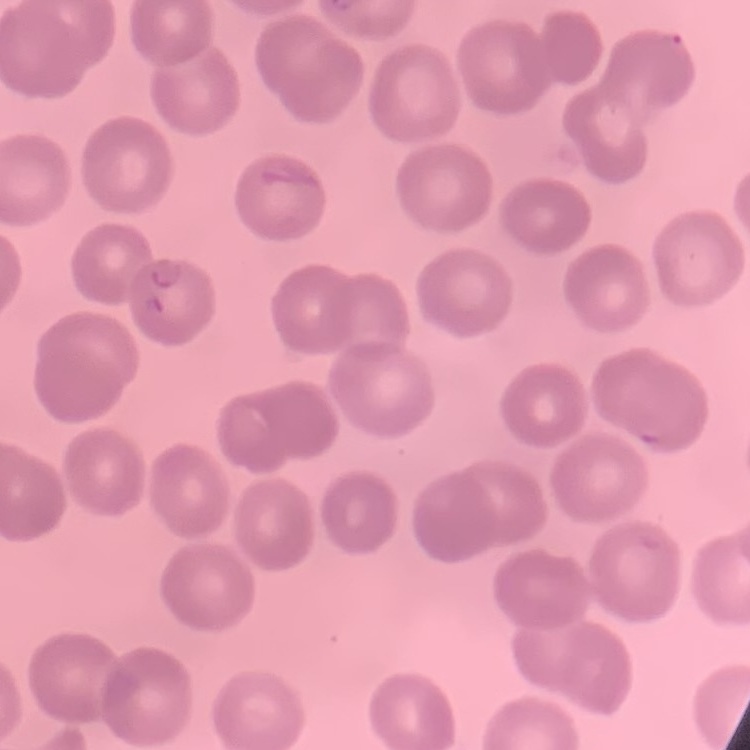
Summary:
  - Erythrocyte morphology: no rouleaux formation
  - Preparation: thin blood film
  - Image type: one tile cut from a larger photomicrograph
  - Stain: Field's or Giemsa